Name the parasite shown.
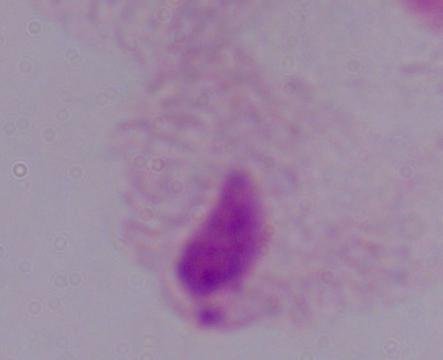
This is a trichomonad.

Captured at 1000x magnification. Photomicrograph.